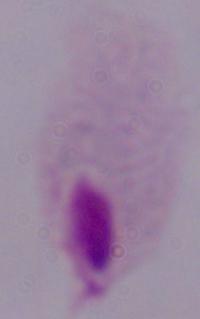
Summary:
  - Modality: micrograph
  - Magnification: 1000x
  - Identification: trichomonad